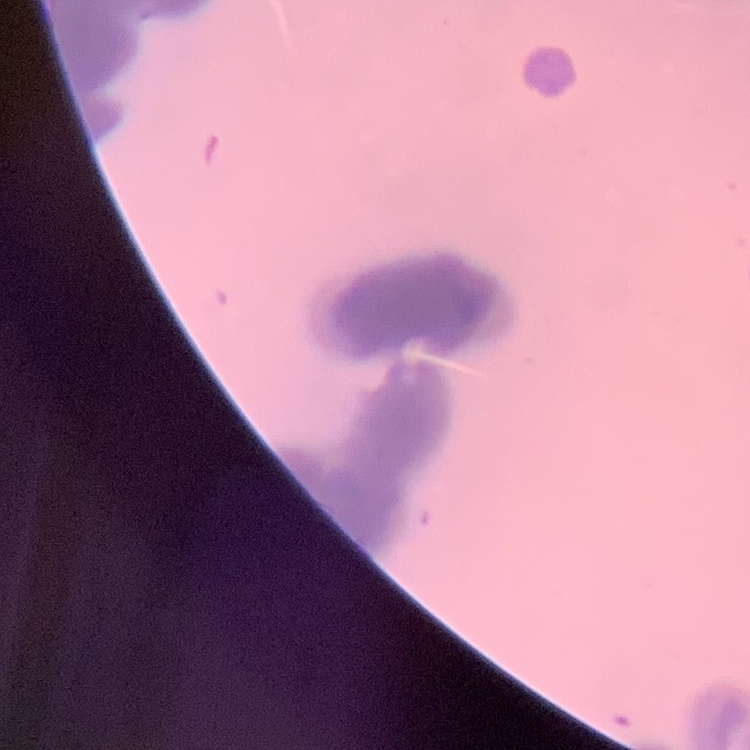
The erythrocytes exhibit rouleaux formation. Stained with either Field's or Giemsa. Thin blood smear. One tile cut from a larger photomicrograph.